Report the malaria status of this cell.
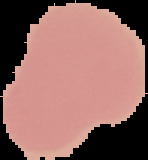

Uninfected.

image size = 148×160 pixels
preparation = thin blood smear
image type = segmented cell region on a black background